Locate every Plasmodium falciparum-infected red blood cell.
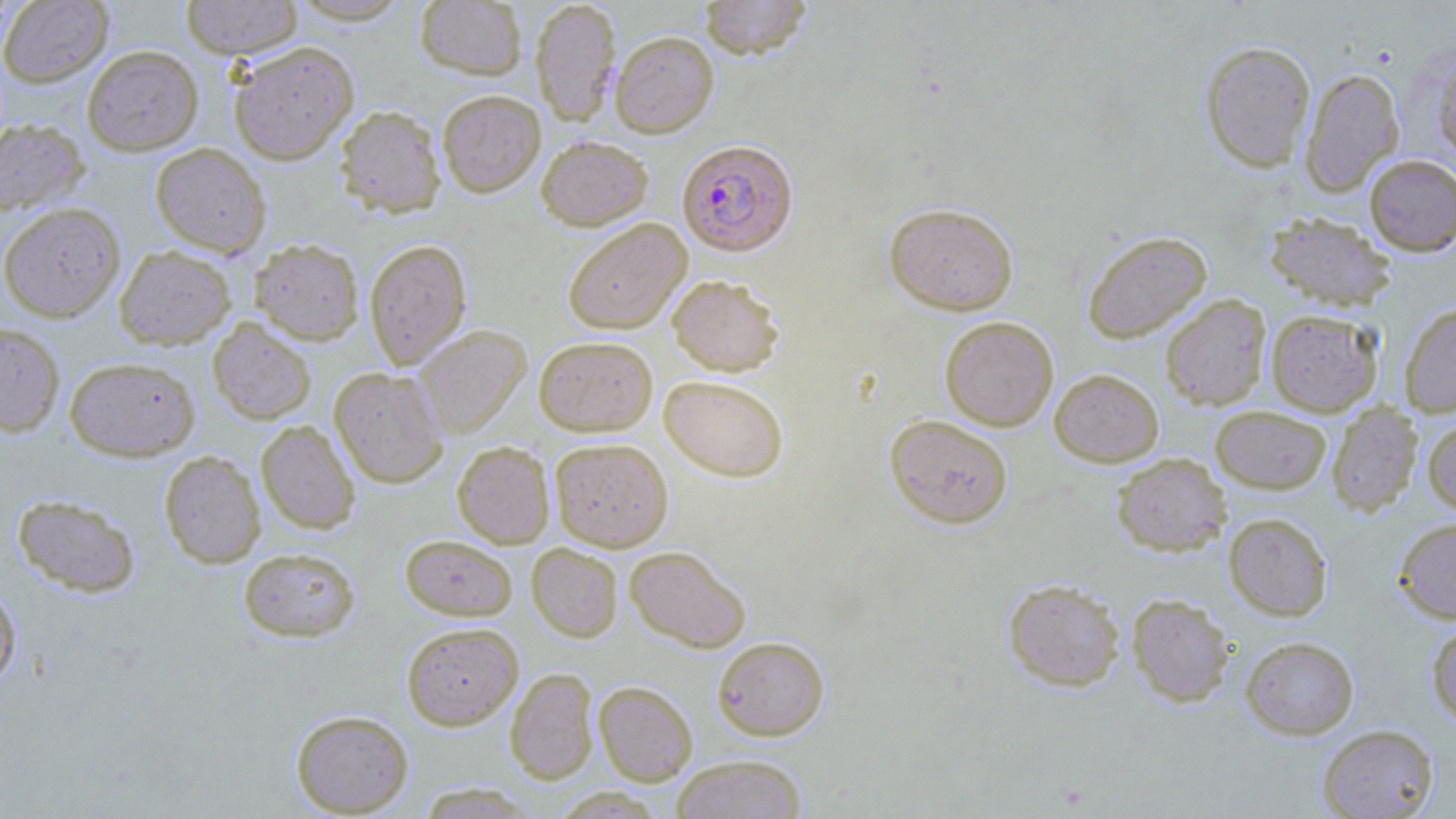
Approximate bounding boxes as (x1, y1, x2, y2) in pixels.
Plasmodium falciparum-infected red blood cells: (677, 139, 798, 256).

Uninfected red blood cell locations: (180, 0, 304, 59), (286, 0, 414, 25), (415, 0, 527, 79), (531, 0, 621, 126), (698, 0, 814, 59), (0, 1, 112, 87), (610, 31, 719, 138), (1200, 40, 1315, 172), (228, 41, 358, 165), (82, 45, 203, 155), (1431, 49, 1456, 162), (1299, 67, 1404, 196), (437, 90, 545, 197), (334, 105, 446, 218), (0, 119, 89, 217), (535, 135, 653, 230), (150, 143, 271, 257), (1363, 154, 1456, 256), (884, 202, 1018, 315), (0, 203, 125, 322), (1264, 211, 1396, 311), (562, 218, 691, 334), (1082, 231, 1212, 344), (250, 238, 364, 345), (364, 239, 472, 370), (114, 245, 236, 349), (667, 274, 784, 376), (1160, 294, 1271, 410), (1400, 301, 1456, 417), (1265, 309, 1383, 416), (940, 316, 1058, 431), (208, 318, 316, 425), (0, 323, 65, 437), (414, 325, 530, 438), (534, 335, 658, 436), (65, 356, 199, 461), (329, 367, 448, 488), (1050, 369, 1164, 467), (659, 375, 788, 482), (1327, 402, 1422, 517), (1210, 406, 1332, 494), (885, 414, 1013, 528), (1423, 416, 1456, 517), (256, 420, 360, 534), (549, 438, 673, 551), (452, 441, 554, 548), (159, 450, 266, 568), (1112, 453, 1231, 556), (12, 493, 140, 597), (1223, 512, 1333, 621), (1393, 517, 1456, 624), (400, 534, 517, 620), (527, 543, 623, 642), (624, 545, 751, 653), (238, 547, 360, 641), (1002, 577, 1125, 692), (0, 582, 22, 689), (1127, 594, 1235, 707), (1426, 621, 1456, 726), (401, 622, 523, 730), (712, 636, 830, 740), (1240, 636, 1359, 739), (505, 667, 599, 784), (594, 681, 697, 786), (290, 709, 414, 816), (1317, 724, 1440, 819), (671, 754, 808, 819). Slide-level diagnosis: Plasmodium falciparum. May-Grünwald-Giemsa-stained preparation. Single field of view. Captured at 1000x magnification. Image is 1456×819 pixels. Light microscopy. Thin blood smear.